Describe the morphology of the red blood cells.
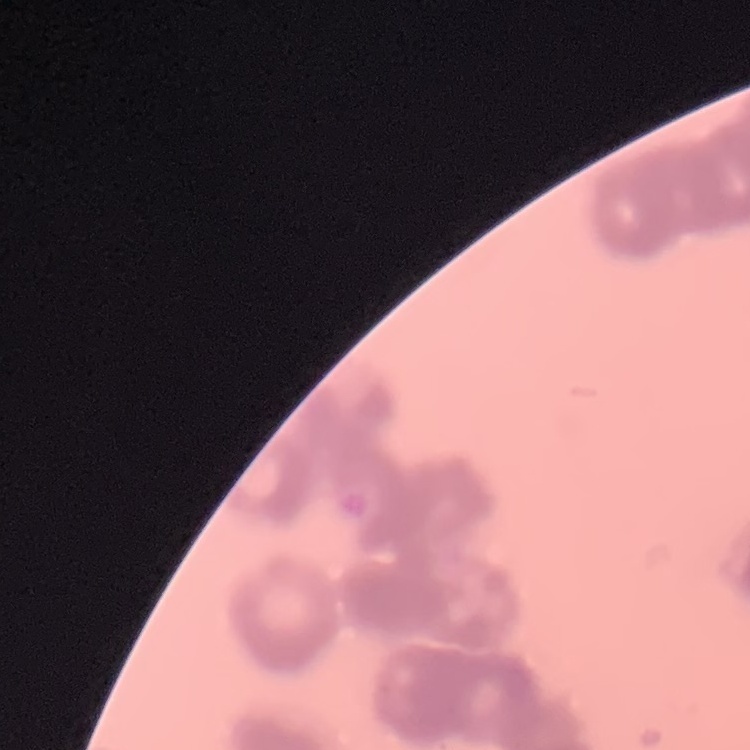

Rouleaux formation.

Summary:
  - Stain: Field's or Giemsa
  - Image type: one tile cut from a larger photomicrograph
  - Preparation: thin blood film